Assess the morphology of the erythrocytes.
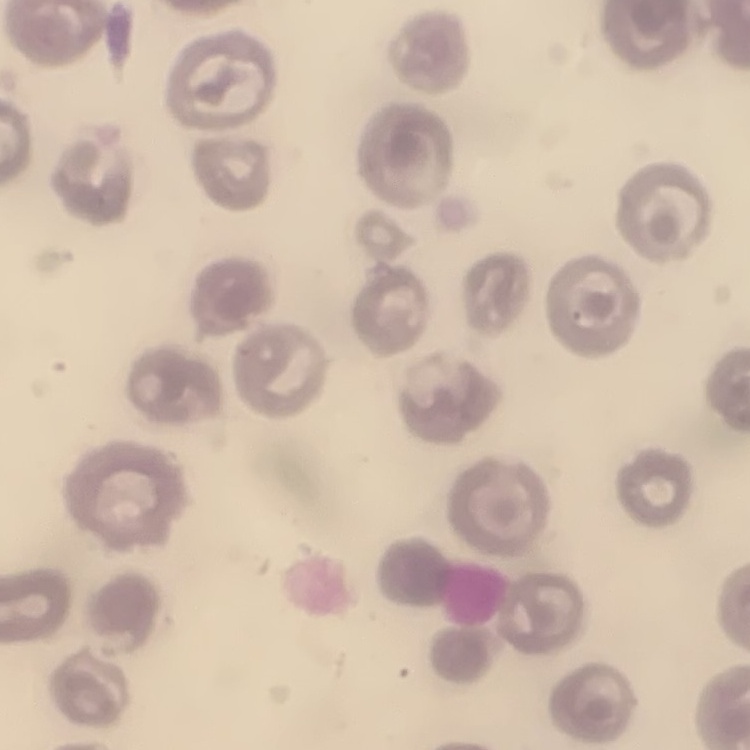

No rouleaux formation.

image type = one tile cut from a larger photomicrograph
preparation = thin blood smear
stain = Field's or Giemsa